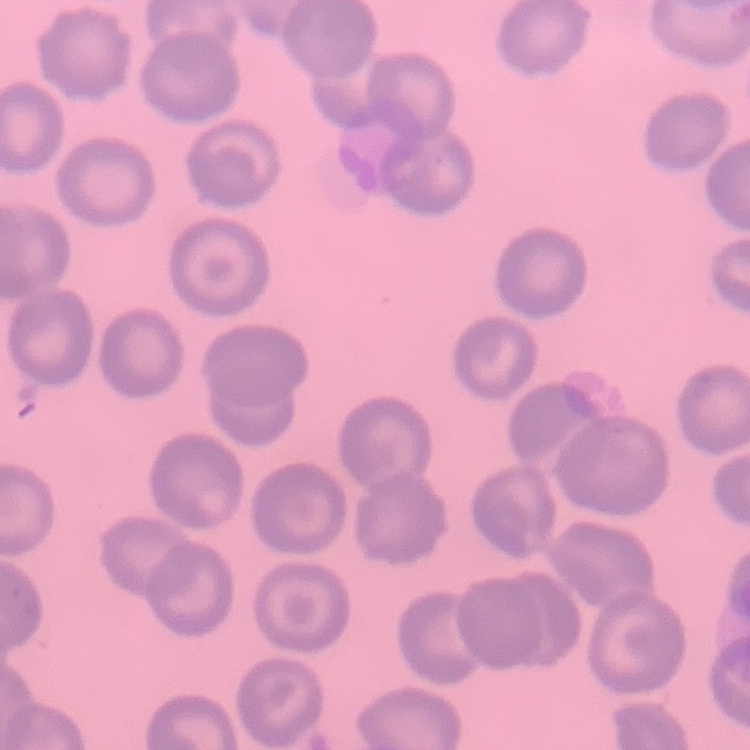

Summary:
  - Red blood cell morphology: no rouleaux formation
  - Stain: Field's or Giemsa
  - Preparation: thin blood smear
  - Image type: square crop of a larger photomicrograph